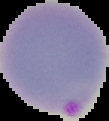
result = malaria parasites detected
image size = 109×121 pixels
preparation = thin blood smear
image type = cell region segmented out of the field of view; surrounding area masked to black